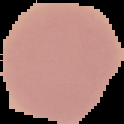
malaria_status: uninfected
preparation: thin blood film
image_type: segmented cell region on a black background
image_size: 124×124 pixels